Identify the parasite.
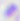
Toxoplasma gondii.

magnification = 400x
modality = micrograph